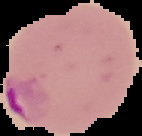
image type = cell region segmented out of the field of view; surrounding area masked to black
malaria status = parasitized
preparation = thin blood smear
image size = 142×136 pixels